Report the malaria status of this cell.
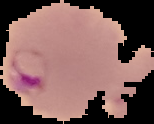
It is parasitized.

preparation: thin blood smear
image_type: cell region segmented out of the field of view; surrounding area masked to black
image_size: 154×124 pixels